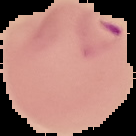
Summary:
  - Image type: cell region segmented out of the field of view; surrounding area masked to black
  - Preparation: thin blood film
  - Image size: 136×136 pixels
  - Malaria status: parasitized